State which parasite is depicted.
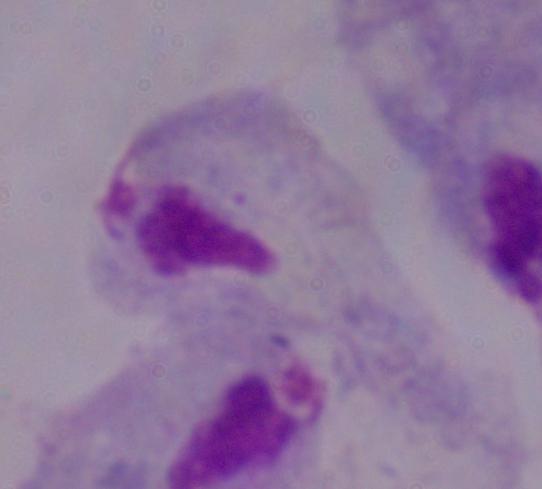

A trichomonad.

modality = photomicrograph
magnification = 1000x